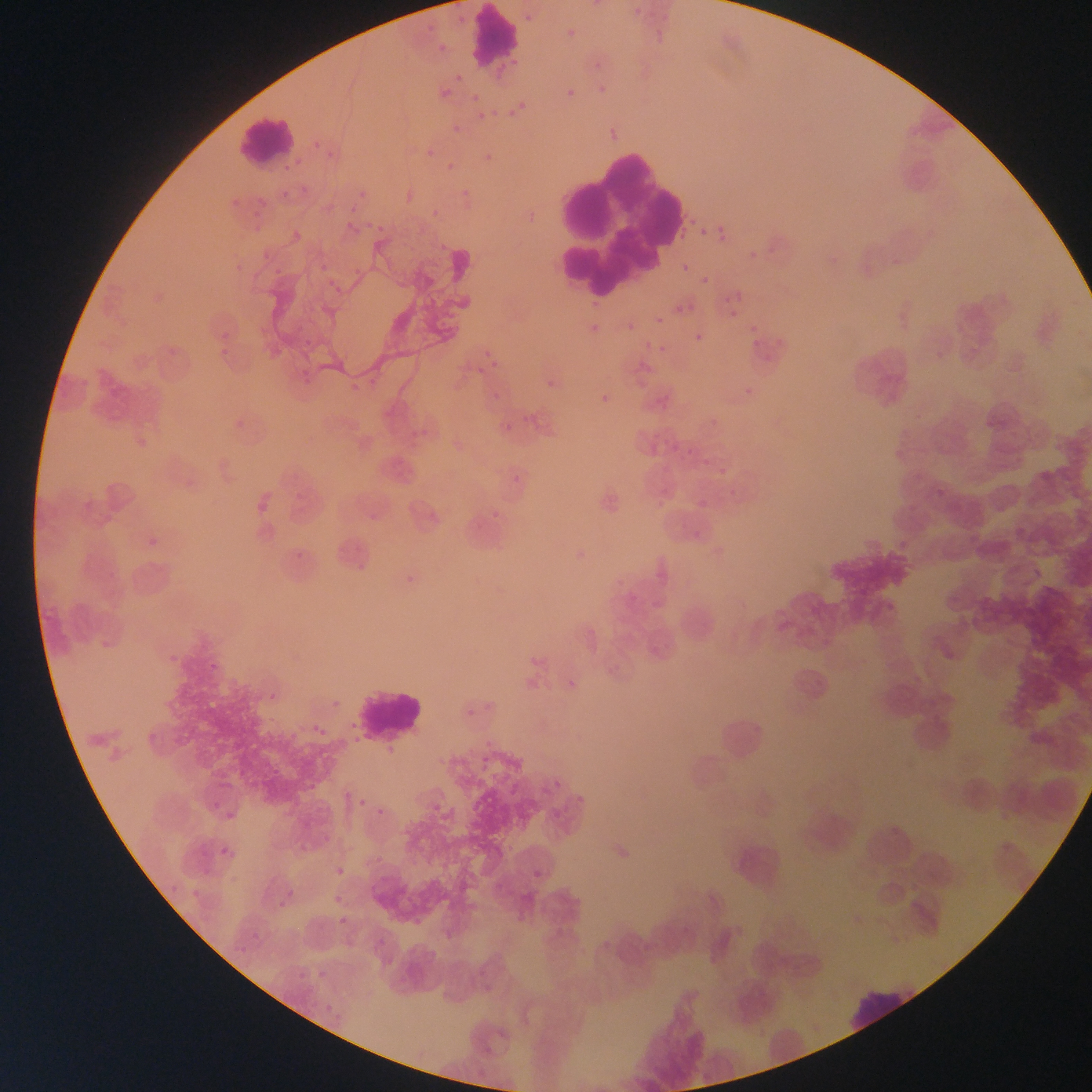

image_size: 1092×1092 pixels
field_of_view: single
plasmodium_parasite_locations: 'approximate bounding boxes as left top right bottom in pixels: 633 7 641 15; 452 13 471 28; 526 14 534 22; 419 20 435 37; 648 21 679 41; 560 27 579 43; 433 38 447 56; 447 67 463 83; 561 78 581 109; 496 83 529 126; 597 87 616 95; 435 89 448 102; 472 93 481 103; 477 111 486 120; 446 123 459 130; 310 138 350 163; 414 144 435 160; 476 151 495 171; 442 162 465 174; 268 177 310 202; 355 182 377 203; 237 189 274 230; 455 189 469 199; 338 201 354 214; 422 205 443 219; 343 218 361 240; 363 220 391 233; 712 221 733 250; 676 222 698 243; 700 227 708 235; 277 229 307 245; 743 234 770 261; 234 246 275 275; 304 258 329 274; 348 263 365 277; 682 263 690 273; 322 269 347 299; 700 276 709 285; 735 291 743 300; 674 306 682 314; 729 310 738 319; 589 314 604 335; 655 316 663 324; 210 317 243 361; 750 325 759 334; 281 327 316 351; 695 333 704 342; 627 338 659 366; 752 339 760 347; 466 348 500 370; 294 357 319 388; 545 369 566 385; 340 375 374 399; 736 382 757 400; 488 384 506 404; 589 393 611 408; 482 407 528 444; 986 420 996 429; 664 426 686 460; 701 458 709 467; 1001 463 1009 471; 712 466 730 482; 512 475 520 484; 491 510 499 518; 694 530 702 538; 144 534 164 555; 285 539 316 562; 351 553 376 572; 398 565 422 584; 162 650 184 675; 204 653 234 669; 260 671 285 703; 306 725 322 737; 354 797 367 808; 209 804 250 835; 375 811 391 824; 195 832 242 873; 322 833 333 846; 332 868 348 881; 335 895 343 903; 275 896 303 914; 242 912 277 946; 339 916 348 925; 295 965 314 979; 319 986 353 1029 | approximate x y pixel centers of objects too small to bound: 601 68'
country: Ghana
leukocyte_locations: 'approximate bounding boxes as left top right bottom in pixels: 468 7 519 67; 236 115 299 167; 552 147 673 288; 351 683 427 741; 843 984 920 1031'
capture: mobile-phone photograph through a microscope
preparation: thin blood smear